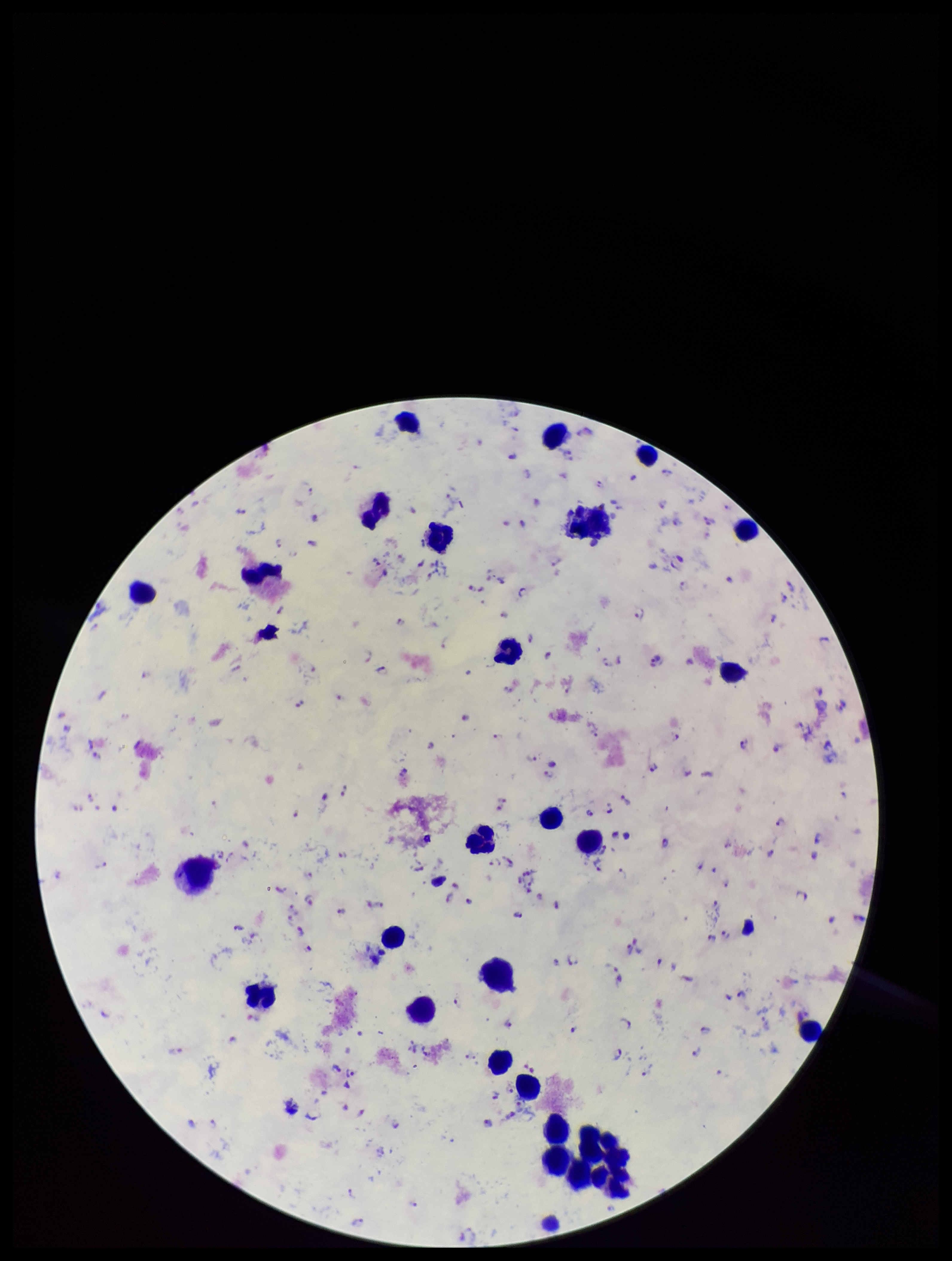
field of view = single
species reported for this patient = Plasmodium falciparum
preparation = thick blood smear
image size = 952×1261 pixels
leukocyte count = 27
capture = smartphone photograph through the microscope eyepiece
parasite count = 117
Plasmodium parasites = detected
stain = Giemsa
patient malaria status = positive